Report the malaria status of this cell.
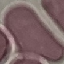
It is uninfected.

{
  "image_type": "cell patch, automatically extracted from a larger field of view and resized to 64 × 64 pixels",
  "stain": "Giemsa",
  "capture": "smartphone through the microscope eyepiece",
  "preparation": "thin blood film"
}